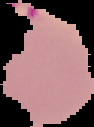

image_size: 94×127 pixels
result: malaria parasites detected
preparation: thin blood smear
image_type: segmented cell region on a black background